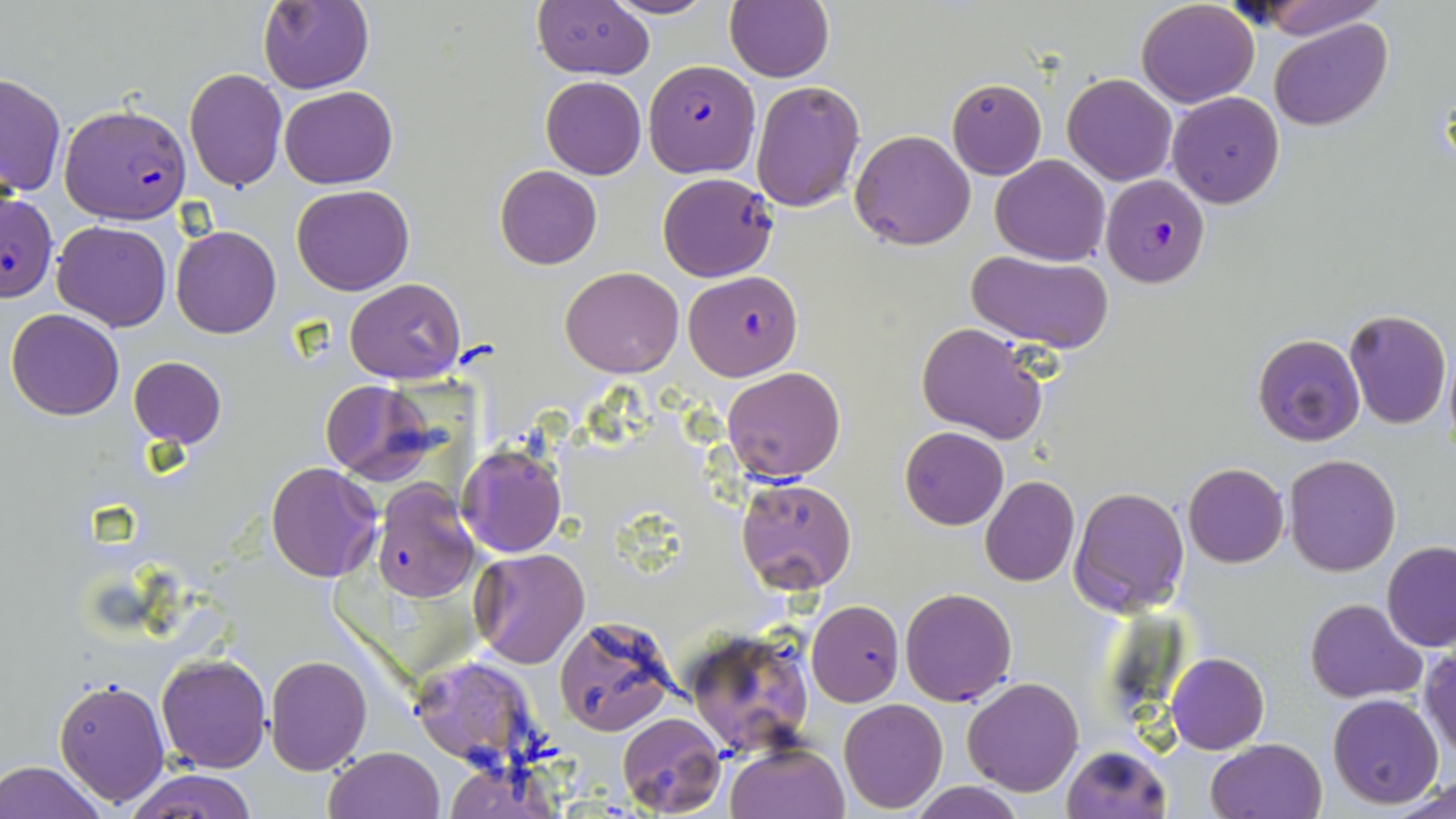
Approximate bounding boxes as named x1/y1/x2/y2 corners in pixels. Uninfected red blood cell locations: (x1=603, y1=0, x2=720, y2=20), (x1=724, y1=0, x2=834, y2=83), (x1=1244, y1=0, x2=1386, y2=38), (x1=258, y1=1, x2=373, y2=93), (x1=532, y1=2, x2=653, y2=79), (x1=1135, y1=2, x2=1259, y2=108), (x1=1270, y1=18, x2=1392, y2=131), (x1=184, y1=67, x2=288, y2=191), (x1=0, y1=72, x2=66, y2=198), (x1=1063, y1=73, x2=1177, y2=186), (x1=541, y1=75, x2=646, y2=178), (x1=946, y1=79, x2=1046, y2=180), (x1=750, y1=80, x2=865, y2=212), (x1=278, y1=86, x2=398, y2=188), (x1=1169, y1=93, x2=1285, y2=208), (x1=849, y1=129, x2=976, y2=251), (x1=990, y1=154, x2=1110, y2=265), (x1=495, y1=166, x2=602, y2=269), (x1=658, y1=173, x2=778, y2=282), (x1=291, y1=185, x2=414, y2=296), (x1=52, y1=220, x2=172, y2=331), (x1=171, y1=225, x2=281, y2=339), (x1=967, y1=249, x2=1113, y2=350), (x1=562, y1=265, x2=683, y2=378), (x1=344, y1=277, x2=467, y2=384), (x1=6, y1=309, x2=124, y2=421), (x1=1344, y1=309, x2=1451, y2=429), (x1=917, y1=321, x2=1050, y2=444), (x1=1253, y1=333, x2=1365, y2=446), (x1=128, y1=357, x2=226, y2=448), (x1=722, y1=365, x2=845, y2=482), (x1=320, y1=380, x2=439, y2=484), (x1=900, y1=427, x2=1008, y2=529), (x1=458, y1=443, x2=567, y2=558), (x1=1284, y1=454, x2=1400, y2=576), (x1=265, y1=462, x2=384, y2=584), (x1=1183, y1=463, x2=1288, y2=567), (x1=979, y1=477, x2=1080, y2=588), (x1=736, y1=478, x2=856, y2=594), (x1=1070, y1=485, x2=1188, y2=616), (x1=1382, y1=541, x2=1456, y2=651), (x1=470, y1=547, x2=590, y2=668), (x1=899, y1=587, x2=1016, y2=706), (x1=1306, y1=598, x2=1427, y2=704), (x1=806, y1=600, x2=904, y2=706), (x1=554, y1=615, x2=677, y2=737), (x1=685, y1=627, x2=813, y2=756), (x1=1420, y1=648, x2=1456, y2=763), (x1=1166, y1=653, x2=1270, y2=754), (x1=156, y1=654, x2=270, y2=774), (x1=265, y1=654, x2=372, y2=775), (x1=408, y1=655, x2=543, y2=773), (x1=54, y1=675, x2=171, y2=808), (x1=961, y1=676, x2=1084, y2=797), (x1=1327, y1=695, x2=1444, y2=808), (x1=838, y1=698, x2=947, y2=814), (x1=617, y1=712, x2=725, y2=818), (x1=1205, y1=738, x2=1327, y2=819), (x1=726, y1=742, x2=848, y2=819), (x1=1062, y1=743, x2=1171, y2=819), (x1=323, y1=747, x2=444, y2=819), (x1=0, y1=760, x2=108, y2=819), (x1=442, y1=760, x2=557, y2=819), (x1=126, y1=769, x2=257, y2=819), (x1=1386, y1=775, x2=1456, y2=818), (x1=910, y1=781, x2=1027, y2=819). Plasmodium falciparum-infected red blood cell locations: (x1=644, y1=60, x2=759, y2=175), (x1=60, y1=103, x2=192, y2=224), (x1=1101, y1=175, x2=1211, y2=288), (x1=0, y1=191, x2=59, y2=303), (x1=684, y1=271, x2=803, y2=381), (x1=370, y1=480, x2=482, y2=602). Slide-level diagnosis: Plasmodium falciparum. Image is 1456×819 pixels. One field of a larger specimen. Thin blood smear. 1000x magnification. May-Grünwald-Giemsa-stained preparation. Light microscopy.